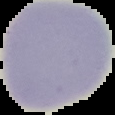
Summary:
  - Image size: 115×115 pixels
  - Malaria status: uninfected
  - Preparation: thin blood smear
  - Image type: segmented cell region on a black background